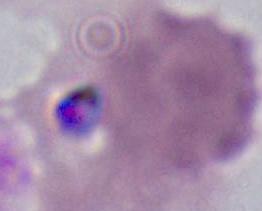
Summary:
  - Identification: Plasmodium
  - Magnification: 400x or 1000x
  - Modality: photomicrograph